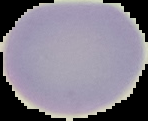

Summary:
  - Image type: cell region segmented out of the field of view; surrounding area masked to black
  - Preparation: thin blood smear
  - Image size: 148×121 pixels
  - Result: no malaria parasites seen